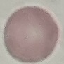
Summary:
  - Result: no malaria parasites seen
  - Stain: Giemsa
  - Preparation: thin blood smear
  - Capture: smartphone through the microscope eyepiece
  - Image type: automatically extracted cell patch, resized to 64 × 64 pixels